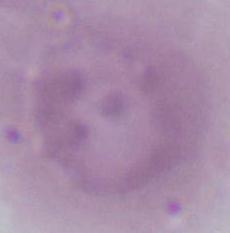
Summary:
  - Modality: micrograph
  - Magnification: 1000x
  - Identification: red blood cell